Outline each blood parasite and name the species.
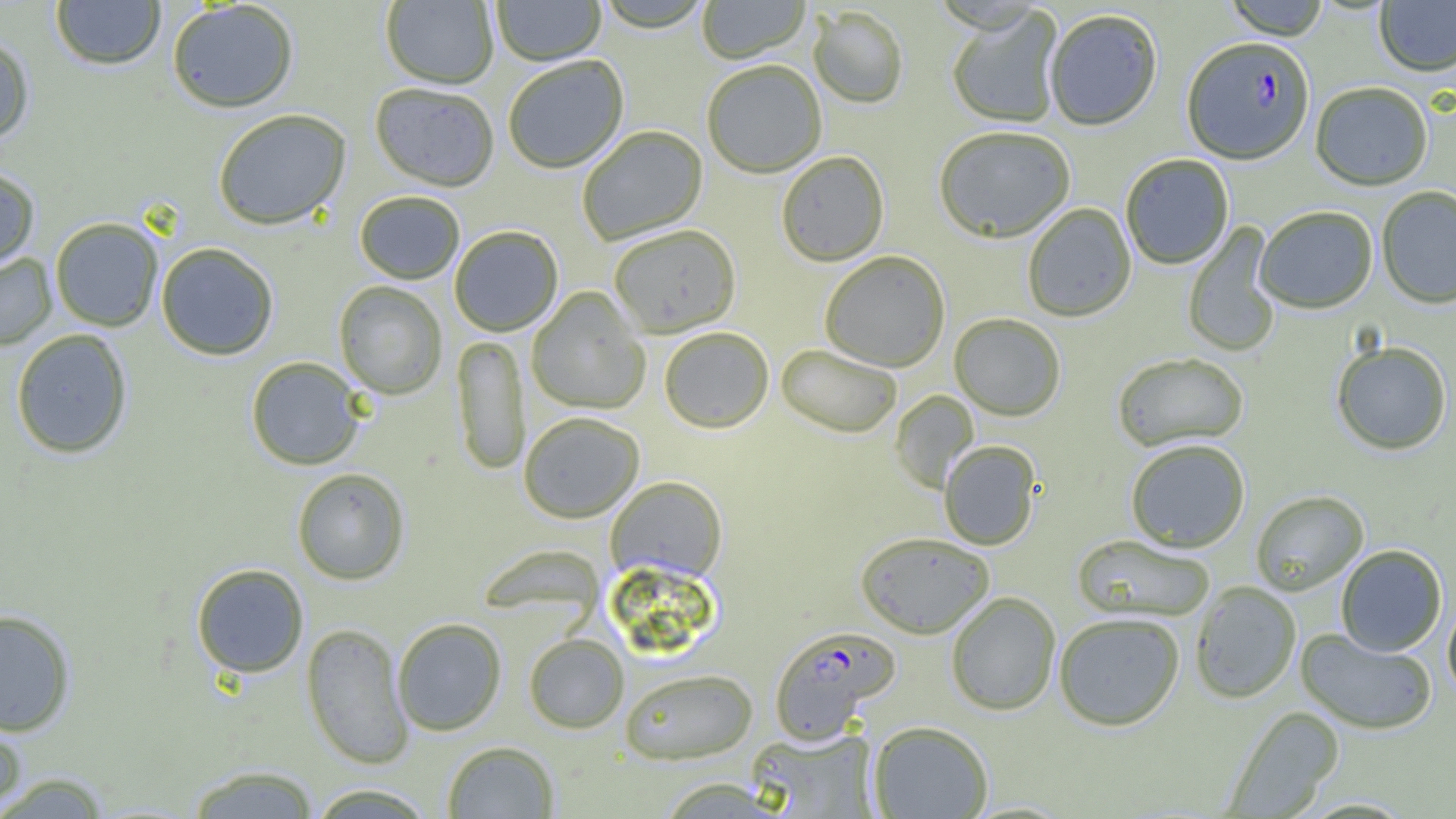

Approximate bounding boxes as [x1, y1, x2, y2] in pixels.
Plasmodium falciparum-infected red blood cells: [1181, 39, 1314, 168], [769, 625, 900, 743].
No Plasmodium ovale, Plasmodium malariae, Plasmodium vivax, Babesia divergens, or Trypanosoma brucei observed.

Uninfected red blood cell locations: [50, 0, 166, 71], [492, 0, 606, 67], [593, 0, 714, 35], [697, 0, 810, 66], [1222, 0, 1330, 42], [1375, 0, 1456, 78], [381, 1, 498, 90], [167, 2, 299, 114], [809, 8, 908, 110], [947, 8, 1064, 130], [1045, 11, 1162, 132], [0, 32, 36, 144], [504, 56, 629, 175], [702, 63, 826, 180], [1310, 84, 1433, 192], [370, 85, 499, 194], [213, 110, 351, 231], [577, 126, 708, 246], [934, 128, 1075, 245], [776, 152, 889, 268], [1121, 155, 1234, 270], [0, 166, 41, 270], [1377, 187, 1456, 311], [354, 191, 465, 285], [1022, 204, 1136, 323], [1254, 208, 1378, 315], [49, 217, 164, 331], [1182, 222, 1282, 358], [450, 226, 563, 337], [609, 226, 741, 339], [156, 243, 278, 361], [0, 251, 57, 351], [820, 252, 950, 373], [334, 281, 447, 399], [527, 287, 650, 415], [949, 314, 1065, 422], [660, 328, 774, 434], [10, 329, 134, 460], [452, 334, 529, 477], [1331, 342, 1452, 456], [776, 345, 901, 438], [1112, 354, 1249, 453], [246, 357, 365, 470], [890, 390, 980, 494], [519, 413, 644, 524], [939, 441, 1040, 550], [1125, 441, 1250, 554], [292, 468, 410, 585], [606, 477, 727, 583], [1251, 491, 1368, 597], [855, 533, 994, 639], [1072, 535, 1215, 623], [476, 545, 607, 623], [1336, 546, 1447, 657], [191, 563, 309, 679], [1190, 582, 1301, 704], [946, 592, 1060, 716], [1443, 599, 1456, 704], [0, 609, 77, 736], [1054, 613, 1184, 732], [392, 618, 507, 736], [302, 622, 414, 769], [1296, 630, 1436, 735], [524, 633, 628, 733], [620, 668, 757, 765], [1222, 706, 1344, 818], [0, 713, 28, 815], [867, 721, 993, 818], [747, 727, 880, 818], [442, 741, 559, 818], [185, 765, 320, 818], [0, 771, 115, 818], [655, 777, 785, 818], [306, 784, 437, 819]. Slide-level diagnosis: Plasmodium falciparum. Captured at 1000x magnification. Single field of view. Optical microscopy. Image is 1456×819 pixels. Thin blood film.